Report the malaria status of this cell.
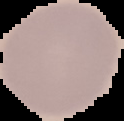

It is uninfected.

Summary:
  - Preparation: thin blood smear
  - Image size: 124×121 pixels
  - Image type: cell region segmented out of the field of view; surrounding area masked to black